Classify this cell by malaria status.
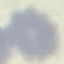

It is uninfected.

Acquired by smartphone through the microscope eyepiece. Thin blood smear. Giemsa stain. Automatically extracted cell patch, resized to 64 × 64 pixels.